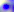
Micrograph. Captured at 400x magnification. Toxoplasma gondii is seen.